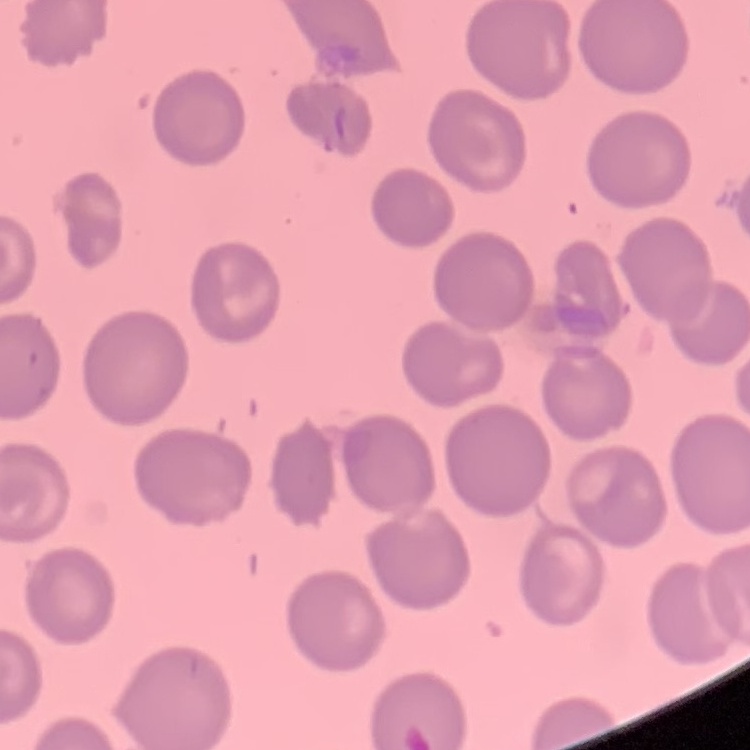

Summary:
  - Erythrocyte morphology: no rouleaux formation
  - Preparation: thin blood film
  - Stain: Field's or Giemsa
  - Image type: square crop of a larger photomicrograph